Name the parasite shown.
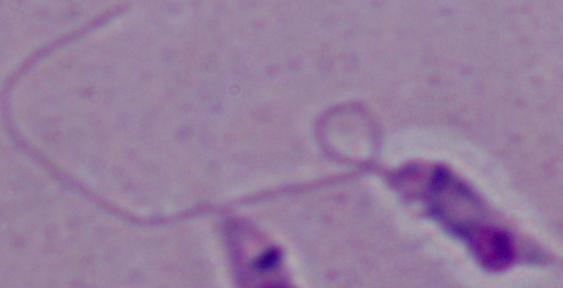
Leishmania.

Summary:
  - Magnification: 1000x
  - Modality: micrograph